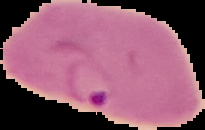
From a thin blood film. Cell region segmented out of the field of view; the surrounding area is masked to black. Image is 205×130 pixels. Result: malaria parasites identified.